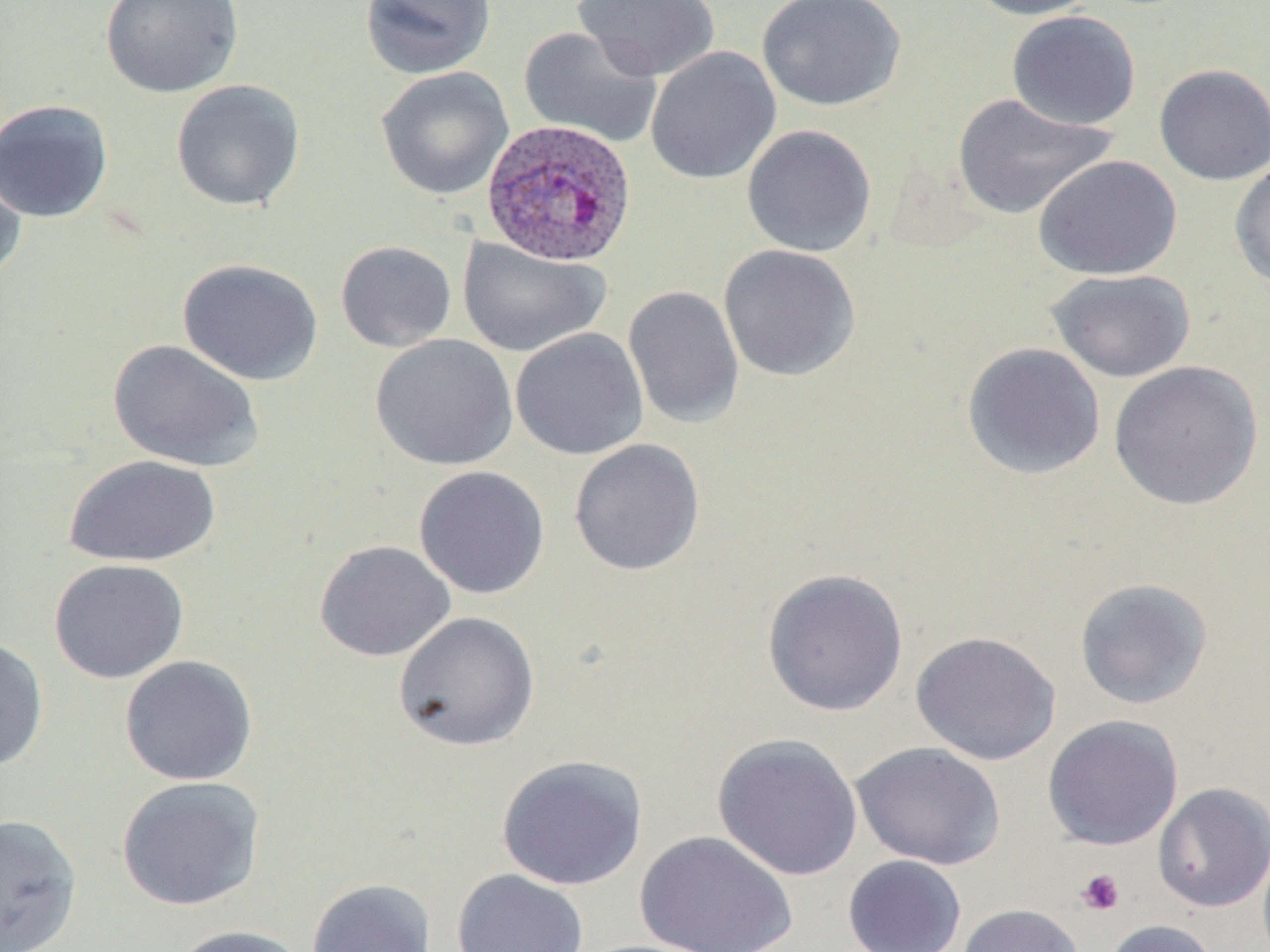
Approximate bounding boxes as (x1, y1, x2, y2) in pixels. Plasmodium ovale-infected red blood cell locations: (482, 119, 637, 267). Uninfected red blood cell locations: (100, 0, 244, 99), (359, 0, 497, 80), (573, 0, 721, 81), (757, 0, 906, 111), (962, 0, 1104, 20), (1006, 10, 1141, 130), (518, 25, 662, 149), (645, 46, 781, 185), (1153, 63, 1270, 186), (376, 66, 514, 200), (170, 79, 306, 212), (952, 92, 1119, 221), (0, 98, 114, 223), (741, 124, 877, 257), (0, 146, 28, 287), (1034, 154, 1182, 280), (1229, 158, 1270, 291), (457, 237, 611, 358), (335, 240, 457, 353), (718, 244, 861, 382), (177, 257, 323, 386), (1045, 268, 1196, 383), (623, 285, 745, 429), (510, 327, 648, 460), (370, 334, 518, 471), (107, 339, 265, 473), (961, 341, 1106, 480), (1108, 360, 1264, 511), (568, 438, 706, 576), (63, 454, 222, 567), (413, 466, 550, 600), (314, 539, 456, 662), (48, 558, 189, 684), (761, 568, 909, 716), (1074, 577, 1214, 709), (393, 611, 540, 751), (910, 630, 1061, 766), (0, 637, 49, 772), (119, 655, 258, 785), (1042, 714, 1184, 850), (712, 733, 863, 881), (850, 741, 1006, 869), (496, 754, 649, 891), (116, 776, 265, 912), (1153, 782, 1270, 912), (0, 813, 83, 952), (634, 830, 799, 952), (842, 855, 967, 952), (451, 868, 590, 952), (305, 878, 438, 952), (955, 903, 1086, 952), (1102, 918, 1221, 952), (169, 924, 313, 952). Platelet locations: (1076, 868, 1125, 916). Slide-level diagnosis: Plasmodium ovale. One field of a larger specimen. May-Grünwald-Giemsa stain. Thin blood smear. 1000x magnification. Light microscopy. Image is 1270×952 pixels.